Assess the morphology of the red blood cells.
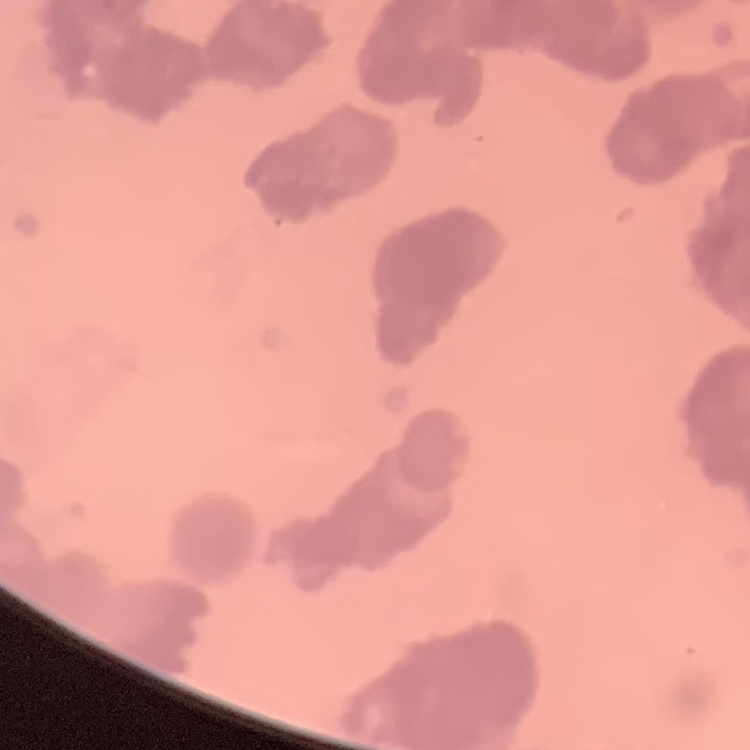

They show rouleaux formation.

preparation: thin blood smear
image_type: one tile cut from a larger photomicrograph
stain: Field's or Giemsa